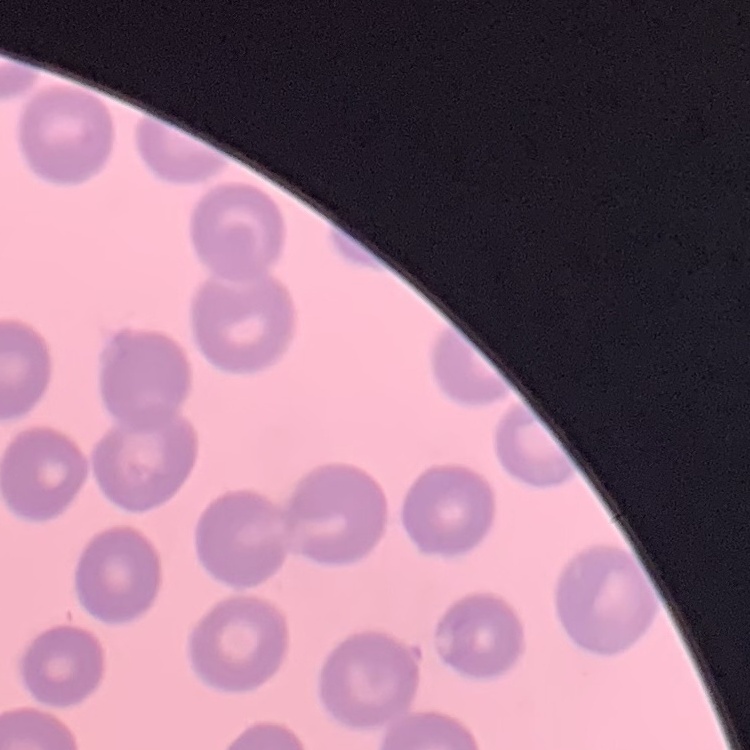

erythrocyte morphology = no rouleaux formation
preparation = thin blood film
image type = one tile cut from a larger photomicrograph
stain = Field's or Giemsa